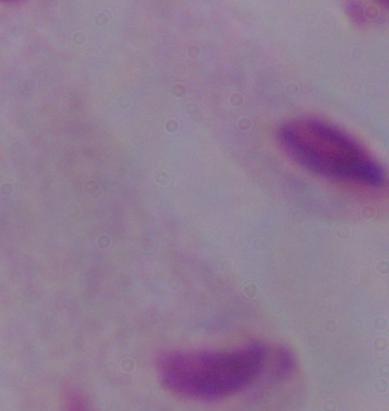

identification = trichomonad
modality = micrograph
magnification = 1000x